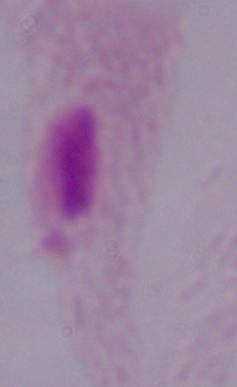

{
  "magnification": "1000x",
  "modality": "photomicrograph",
  "identification": "trichomonad"
}